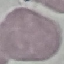

Summary:
  - Result: no malaria parasites seen
  - Image type: automatically extracted cell patch, resized to 64 × 64 pixels
  - Capture: smartphone through the microscope eyepiece
  - Preparation: thin blood film
  - Stain: Giemsa